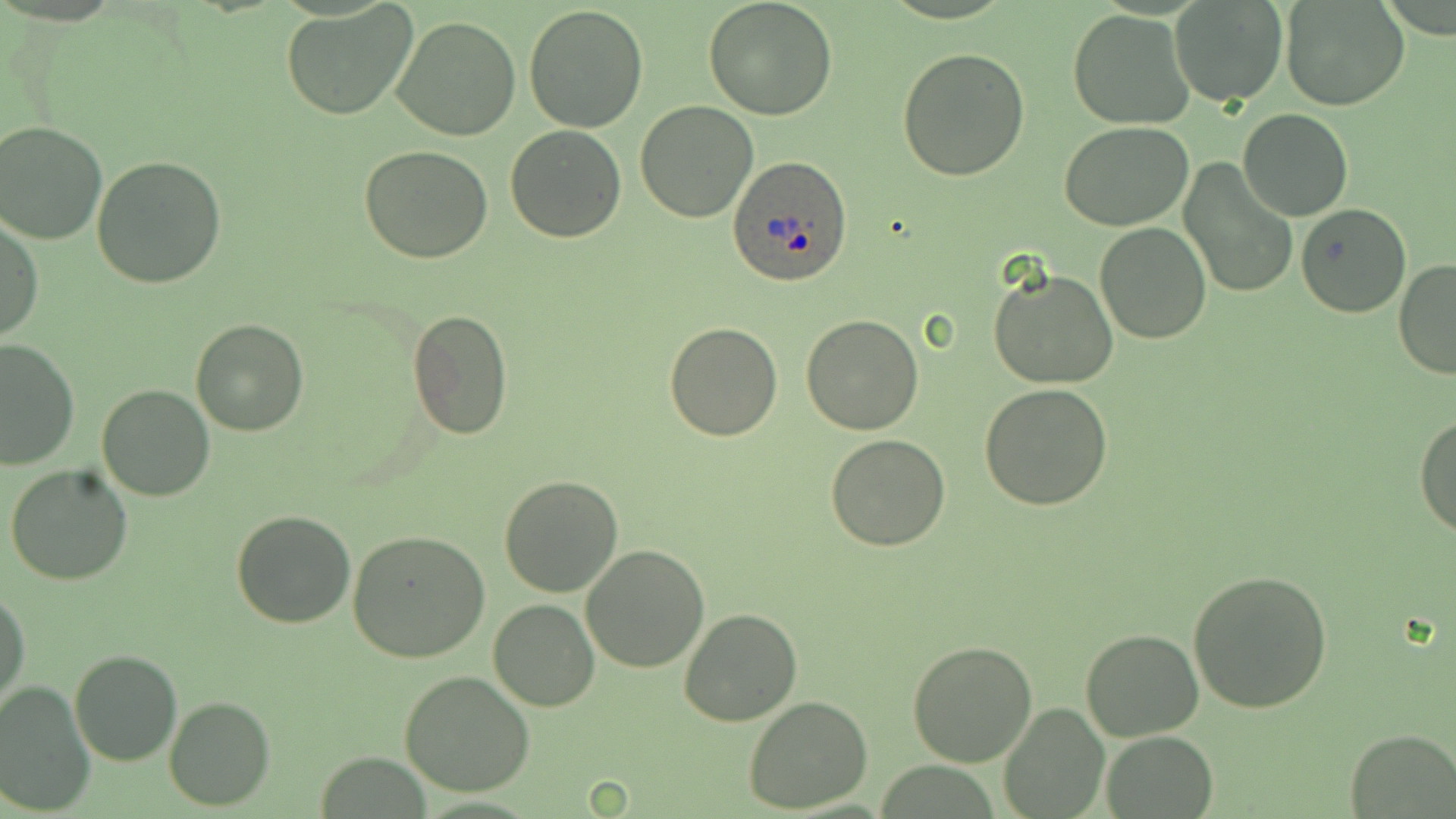

Summary:
  - Coordinate format: approximate bounding boxes as named x1/y1/x2/y2 corners in pixels
  - Plasmodium ovale-infected red blood cell locations: (x1=729, y1=153, x2=854, y2=288)
  - Uninfected red blood cell locations: (x1=702, y1=0, x2=840, y2=119), (x1=1169, y1=1, x2=1288, y2=107), (x1=1282, y1=1, x2=1409, y2=111), (x1=281, y1=2, x2=421, y2=121), (x1=524, y1=3, x2=649, y2=133), (x1=1069, y1=9, x2=1196, y2=129), (x1=391, y1=14, x2=523, y2=141), (x1=897, y1=46, x2=1031, y2=180), (x1=634, y1=100, x2=759, y2=223), (x1=1237, y1=109, x2=1354, y2=222), (x1=0, y1=120, x2=108, y2=244), (x1=1060, y1=121, x2=1194, y2=231), (x1=505, y1=123, x2=629, y2=242), (x1=1203, y1=123, x2=1324, y2=261), (x1=359, y1=143, x2=493, y2=264), (x1=91, y1=156, x2=227, y2=289), (x1=1178, y1=161, x2=1294, y2=299), (x1=1294, y1=201, x2=1413, y2=318), (x1=0, y1=215, x2=42, y2=346), (x1=1095, y1=221, x2=1212, y2=345), (x1=1393, y1=256, x2=1456, y2=380), (x1=987, y1=264, x2=1119, y2=389), (x1=406, y1=308, x2=514, y2=443), (x1=801, y1=314, x2=924, y2=435), (x1=190, y1=319, x2=310, y2=438), (x1=663, y1=321, x2=782, y2=441), (x1=0, y1=336, x2=79, y2=471), (x1=95, y1=382, x2=216, y2=501), (x1=978, y1=383, x2=1113, y2=511), (x1=1415, y1=412, x2=1456, y2=539), (x1=825, y1=433, x2=950, y2=551), (x1=5, y1=464, x2=132, y2=586), (x1=499, y1=474, x2=623, y2=597), (x1=230, y1=509, x2=356, y2=629), (x1=347, y1=529, x2=490, y2=664), (x1=580, y1=543, x2=710, y2=672), (x1=1188, y1=567, x2=1333, y2=713), (x1=1, y1=588, x2=29, y2=713), (x1=488, y1=599, x2=599, y2=712), (x1=678, y1=608, x2=804, y2=728), (x1=1080, y1=629, x2=1204, y2=741), (x1=906, y1=641, x2=1038, y2=768), (x1=68, y1=649, x2=182, y2=766), (x1=0, y1=670, x2=179, y2=793), (x1=398, y1=670, x2=536, y2=796), (x1=0, y1=681, x2=95, y2=815), (x1=163, y1=696, x2=276, y2=812), (x1=743, y1=697, x2=873, y2=813), (x1=998, y1=703, x2=1111, y2=818), (x1=1343, y1=730, x2=1456, y2=817), (x1=1099, y1=732, x2=1218, y2=817)
  - Slide-level diagnosis: Plasmodium ovale
  - Preparation: thin blood smear
  - Stain: May-Grünwald-Giemsa
  - Magnification: 1000x
  - Modality: light microscopy
  - Field of view: single
  - Image size: 1456×819 pixels